Name the cell type shown.
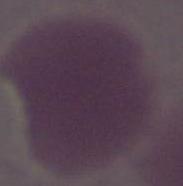

An erythrocyte.

modality = micrograph
magnification = 1000x